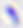
{
  "modality": "micrograph",
  "identification": "Toxoplasma gondii",
  "magnification": "400x"
}